Name the parasite shown.
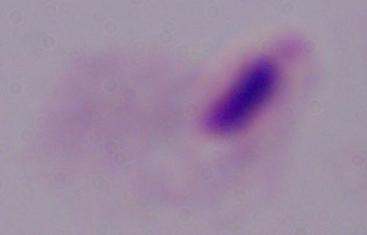

A trichomonad.

Summary:
  - Modality: photomicrograph
  - Magnification: 1000x